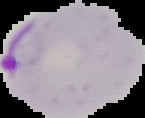

Summary:
  - Image size: 145×118 pixels
  - Preparation: thin blood film
  - Result: malaria parasites detected
  - Image type: segmented cell region with the area outside set to black